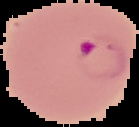 Malaria status: parasitized. Cell region segmented out of the field of view; the surrounding area is masked to black. Image is 139×127 pixels. From a thin blood smear.